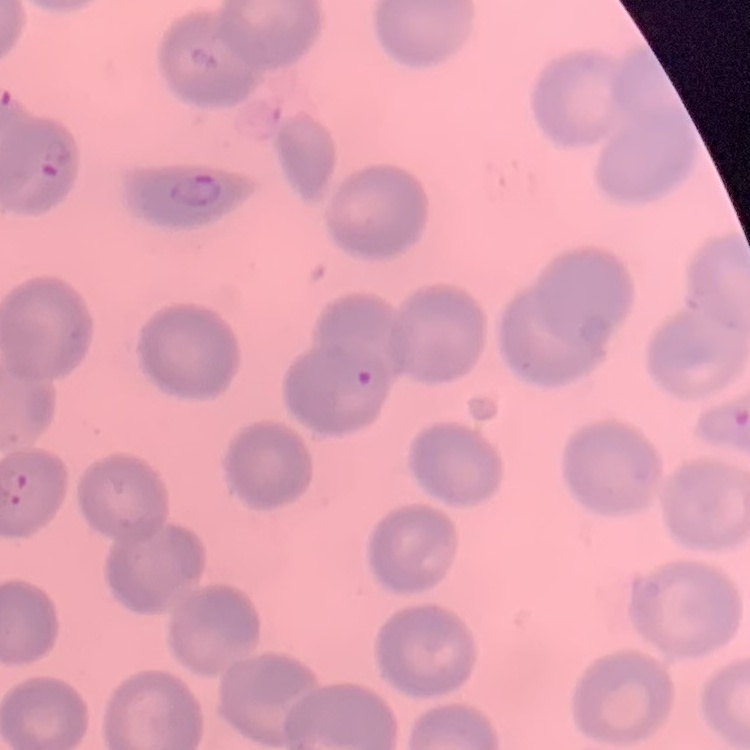
erythrocyte morphology = no rouleaux formation
image type = one tile cut from a larger photomicrograph
stain = Field's or Giemsa
preparation = thin peripheral smear